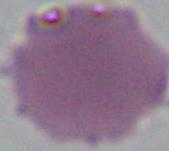
{
  "modality": "micrograph",
  "identification": "erythrocyte",
  "magnification": "1000x"
}